State which cell type is depicted.
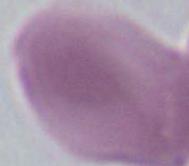
This is an erythrocyte.

modality = micrograph
magnification = 1000x